Assess the background quality.
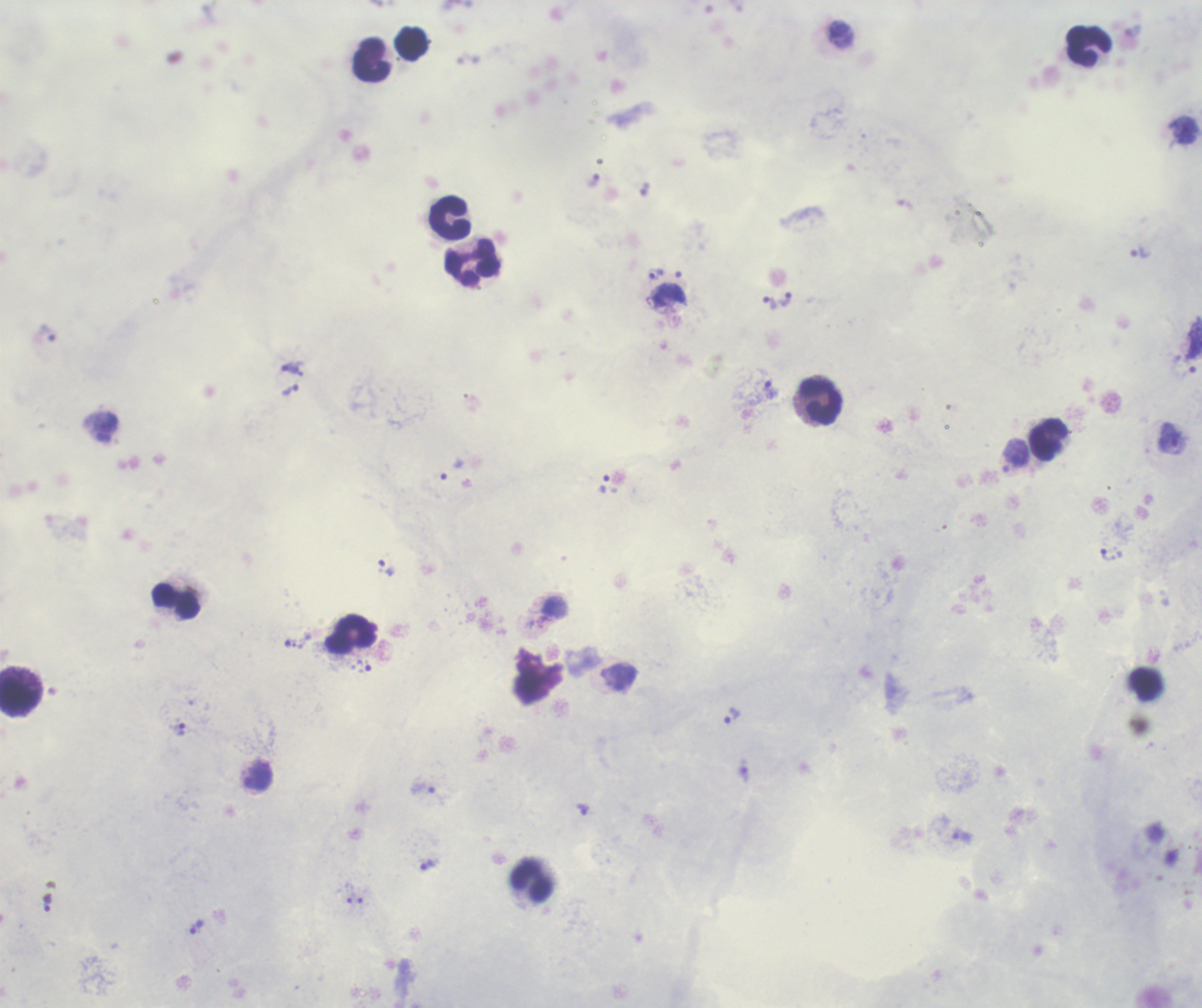

Satisfactory.

Approximate object centers, in pixels from the top-left corner. Trophozoite locations: (x=1139, y=253), (x=655, y=274), (x=786, y=299), (x=769, y=303), (x=289, y=366), (x=771, y=389), (x=290, y=391), (x=1173, y=438), (x=1108, y=555), (x=387, y=567), (x=731, y=715), (x=181, y=729), (x=583, y=809), (x=425, y=864), (x=48, y=903), (x=196, y=927). Leukocyte locations: (x=1089, y=46), (x=371, y=59), (x=449, y=218), (x=472, y=262), (x=821, y=401), (x=1048, y=440), (x=176, y=601), (x=352, y=634), (x=1146, y=685), (x=19, y=695), (x=532, y=880). Previously used in an actual diagnosis. Captured at 100x magnification. Single field of view. Coloration quality: good. Thick blood smear. Image is 1202×1008 pixels. Romanowsky-stained preparation. Result: Plasmodium parasites identified.